Name the parasite shown.
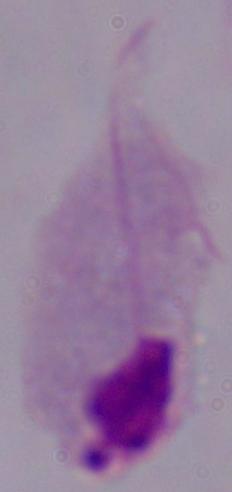
This is a trichomonad.

Photomicrograph. Captured at 1000x magnification.